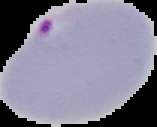

Summary:
  - Image type: segmented cell region with the area outside set to black
  - Preparation: thin blood film
  - Malaria status: parasitized
  - Image size: 157×127 pixels